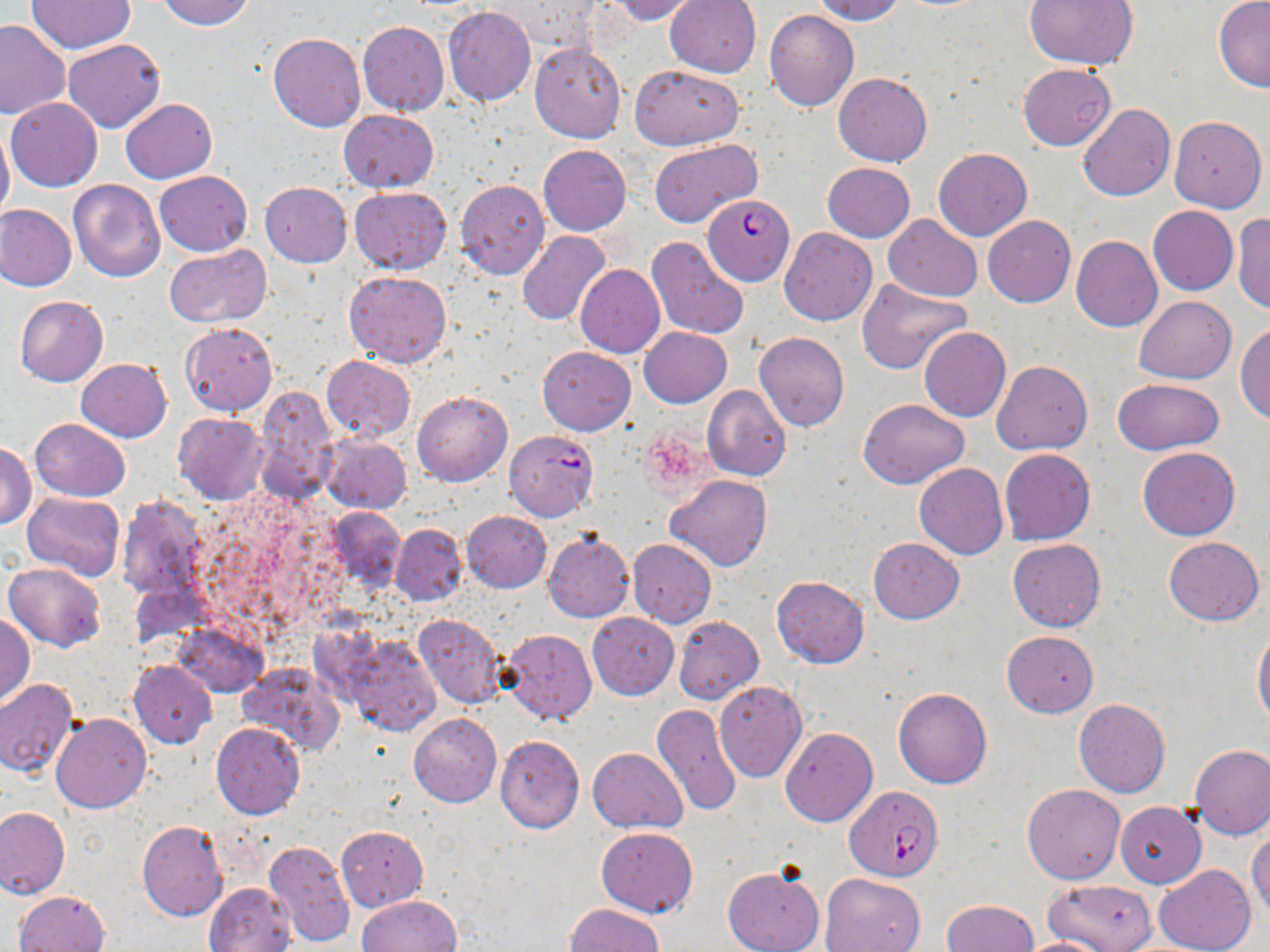

Approximate bounding boxes as [x1, y1, x2, y2] in pixels. Plasmodium falciparum-infected red blood cell locations: [702, 195, 792, 283], [844, 786, 945, 881]. Uninfected red blood cell locations: [156, 0, 256, 30], [487, 0, 602, 56], [606, 0, 705, 24], [664, 0, 761, 77], [811, 0, 905, 24], [1214, 0, 1270, 91], [26, 1, 136, 53], [1024, 1, 1138, 71], [442, 7, 535, 105], [765, 10, 860, 111], [0, 19, 70, 118], [357, 21, 449, 116], [268, 32, 365, 132], [63, 40, 166, 133], [529, 41, 626, 142], [1018, 63, 1117, 151], [629, 64, 744, 150], [834, 73, 932, 166], [6, 98, 102, 192], [119, 98, 217, 182], [1078, 104, 1175, 201], [339, 110, 438, 192], [1168, 114, 1266, 212], [0, 120, 15, 225], [649, 139, 762, 230], [538, 145, 631, 235], [932, 147, 1032, 240], [823, 163, 915, 241], [154, 170, 251, 257], [67, 179, 166, 281], [455, 179, 550, 278], [260, 182, 351, 266], [349, 187, 452, 274], [0, 205, 76, 291], [1148, 206, 1238, 295], [1231, 213, 1270, 314], [883, 215, 982, 300], [983, 215, 1075, 307], [779, 227, 877, 326], [516, 229, 612, 326], [1070, 235, 1162, 331], [646, 237, 750, 340], [163, 246, 271, 328], [575, 265, 666, 358], [344, 270, 452, 366], [856, 281, 972, 373], [13, 296, 108, 387], [1134, 296, 1236, 384], [180, 322, 277, 416], [1236, 323, 1270, 426], [638, 327, 731, 407], [918, 327, 1010, 422], [753, 332, 849, 433], [537, 347, 635, 435], [321, 355, 414, 442], [75, 358, 171, 442], [991, 360, 1092, 455], [1112, 379, 1225, 454], [702, 385, 792, 481], [254, 386, 339, 505], [412, 391, 513, 486], [858, 398, 968, 487], [173, 412, 268, 505], [30, 419, 130, 502], [503, 430, 599, 520], [320, 434, 412, 513], [1, 443, 36, 527], [1138, 446, 1240, 541], [999, 448, 1095, 544], [913, 463, 1008, 560], [666, 475, 772, 571], [21, 491, 126, 581], [114, 494, 212, 602], [323, 507, 404, 595], [462, 510, 551, 592], [389, 523, 466, 606], [542, 531, 635, 622], [1163, 536, 1263, 626], [869, 537, 964, 624], [1007, 538, 1106, 632], [627, 539, 716, 627], [4, 563, 106, 652], [771, 576, 870, 668], [1, 611, 34, 707], [586, 612, 678, 699], [412, 613, 511, 710], [674, 616, 765, 705], [173, 621, 267, 697], [1253, 626, 1270, 731], [500, 628, 597, 726], [1001, 630, 1099, 718], [342, 634, 440, 737], [128, 660, 216, 747], [237, 662, 345, 756], [0, 678, 79, 778], [714, 681, 807, 781], [892, 688, 992, 788], [1073, 699, 1170, 798], [652, 703, 742, 818], [408, 713, 501, 808], [52, 714, 151, 814], [211, 723, 305, 820], [780, 727, 878, 827], [495, 735, 585, 833], [1188, 744, 1270, 839], [588, 747, 688, 832], [1022, 784, 1126, 884], [1115, 802, 1205, 888], [0, 807, 69, 898], [137, 819, 227, 921], [336, 825, 428, 910], [595, 827, 698, 916], [1248, 827, 1270, 923], [264, 840, 354, 946], [721, 864, 824, 952], [1153, 865, 1255, 952], [819, 873, 927, 951], [1043, 878, 1159, 952], [204, 882, 295, 952], [13, 889, 109, 952], [356, 894, 462, 952], [941, 899, 1038, 951], [565, 903, 663, 952], [1012, 937, 1111, 952]. Slide-level diagnosis: Plasmodium falciparum. One field of a larger specimen. May-Grünwald-Giemsa stain. Optical microscopy. Thin blood smear. Image is 1270×952 pixels. Captured at 1000x magnification.